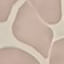
Summary:
  - Result: negative for malaria parasites
  - Capture: smartphone through the microscope eyepiece
  - Preparation: thin blood smear
  - Stain: Giemsa
  - Image type: cell patch, automatically extracted from a larger field of view and resized to 64 × 64 pixels